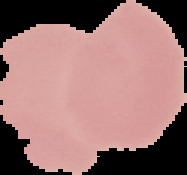
{
  "image_size": "187×175 pixels",
  "malaria_status": "uninfected",
  "preparation": "thin blood smear",
  "image_type": "segmented cell region with the area outside set to black"
}